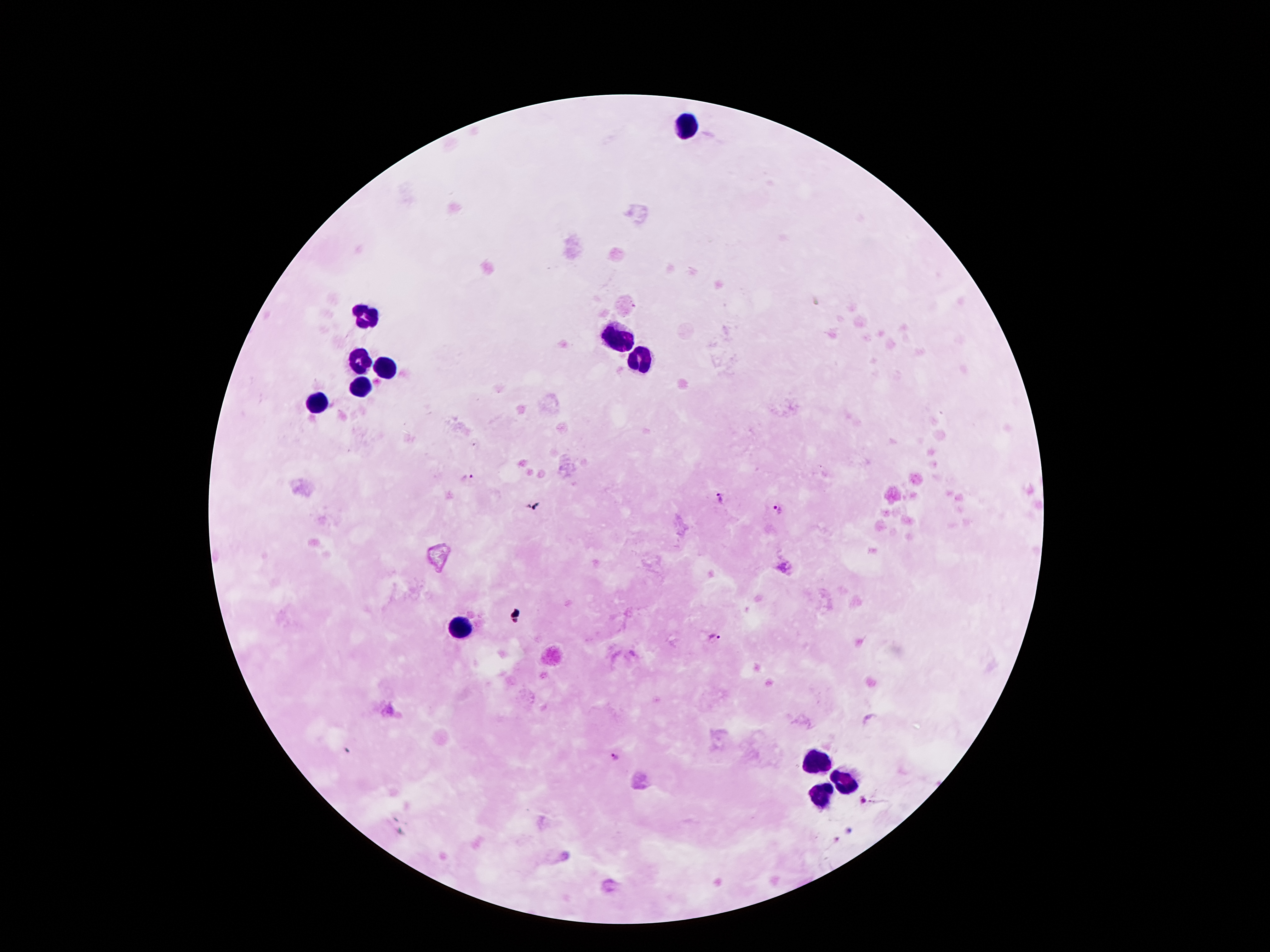 Approximate object centers, in pixels from the top-left corner. Leukocyte locations: (x=685, y=122), (x=364, y=315), (x=620, y=337), (x=637, y=359), (x=360, y=360), (x=383, y=367), (x=360, y=390), (x=316, y=406), (x=459, y=626), (x=813, y=762), (x=845, y=781), (x=820, y=794). Plasmodium parasite locations: (x=469, y=475), (x=721, y=498), (x=776, y=509), (x=714, y=637), (x=613, y=757), (x=862, y=801). Thick blood film. Image is 1270×952 pixels. Photographed through the microscope eyepiece with a smartphone camera. Single field of view. Giemsa-stained preparation. 100x magnification. Patient malaria status: infected with Plasmodium falciparum.